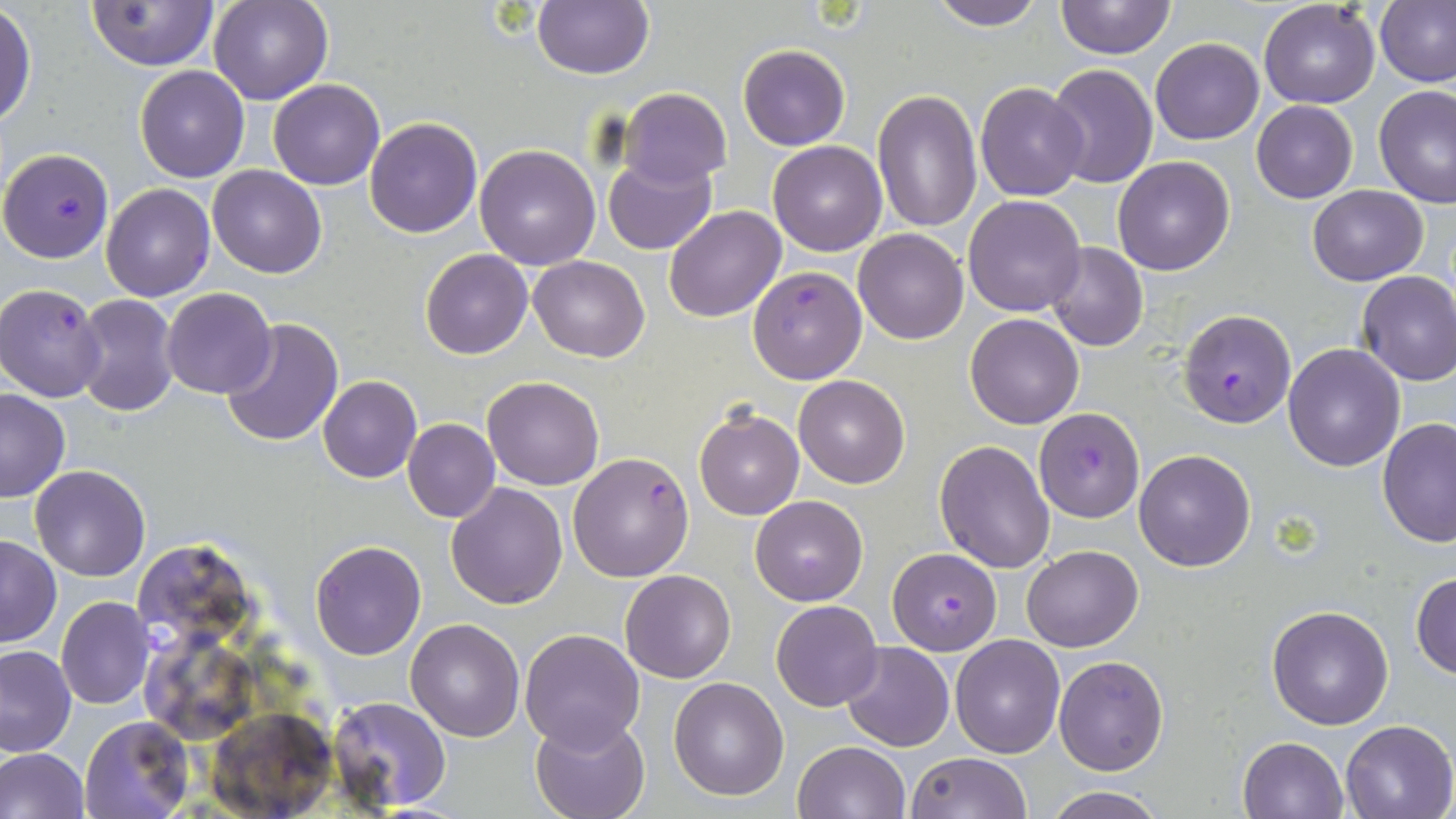
Summary:
  - Coordinate format: approximate bounding boxes as (x1, y1, x2, y2) in pixels
  - Plasmodium falciparum-infected red blood cell locations: (2, 146, 115, 263), (747, 265, 868, 383), (0, 282, 107, 401), (1178, 308, 1297, 428), (1034, 408, 1143, 524), (566, 451, 695, 581), (887, 547, 1002, 655)
  - Uninfected red blood cell locations: (208, 0, 332, 104), (532, 0, 653, 80), (928, 0, 1047, 30), (1055, 0, 1175, 60), (1258, 0, 1381, 109), (1377, 0, 1455, 88), (87, 1, 219, 71), (0, 5, 36, 130), (1150, 36, 1264, 145), (737, 43, 851, 150), (1047, 63, 1157, 188), (135, 66, 250, 183), (268, 78, 385, 191), (975, 82, 1089, 200), (1373, 85, 1456, 210), (620, 90, 730, 185), (872, 90, 983, 234), (1250, 100, 1358, 203), (365, 117, 482, 238), (768, 139, 888, 256), (475, 142, 601, 269), (603, 155, 715, 256), (1113, 156, 1234, 274), (208, 165, 326, 278), (101, 183, 215, 300), (1307, 185, 1430, 285), (962, 194, 1087, 317), (662, 206, 786, 323), (853, 228, 969, 345), (1047, 241, 1148, 351), (421, 248, 532, 359), (529, 254, 650, 362), (1355, 269, 1456, 385), (161, 287, 276, 399), (73, 294, 180, 417), (965, 313, 1085, 429), (221, 318, 344, 448), (1281, 342, 1406, 470), (318, 375, 421, 483), (483, 375, 604, 490), (794, 375, 909, 489), (0, 387, 71, 502), (694, 406, 804, 520), (1378, 417, 1456, 550), (403, 418, 499, 522), (934, 441, 1054, 572), (1133, 448, 1256, 572), (30, 464, 150, 582), (445, 482, 567, 609), (749, 495, 869, 605), (1, 535, 61, 646), (310, 539, 426, 659), (135, 542, 248, 651), (1022, 544, 1144, 652), (620, 569, 736, 683), (1411, 571, 1456, 678), (56, 596, 154, 709), (770, 600, 883, 712), (1267, 605, 1393, 729), (405, 617, 525, 740), (519, 627, 646, 750), (950, 635, 1066, 757), (140, 639, 260, 738), (839, 641, 953, 751), (0, 645, 76, 757), (1054, 655, 1169, 776), (667, 676, 790, 801), (327, 696, 453, 810), (204, 709, 336, 816), (530, 715, 652, 819), (78, 716, 194, 818), (1339, 719, 1455, 819), (1238, 735, 1348, 818), (792, 740, 909, 819), (0, 747, 89, 819), (905, 752, 1033, 819), (1042, 785, 1166, 818)
  - Slide-level diagnosis: Plasmodium falciparum
  - Preparation: thin blood film
  - Stain: May-Grünwald-Giemsa
  - Field of view: single
  - Magnification: 1000x
  - Image size: 1456×819 pixels
  - Modality: light microscopy